Name the blood parasite species.
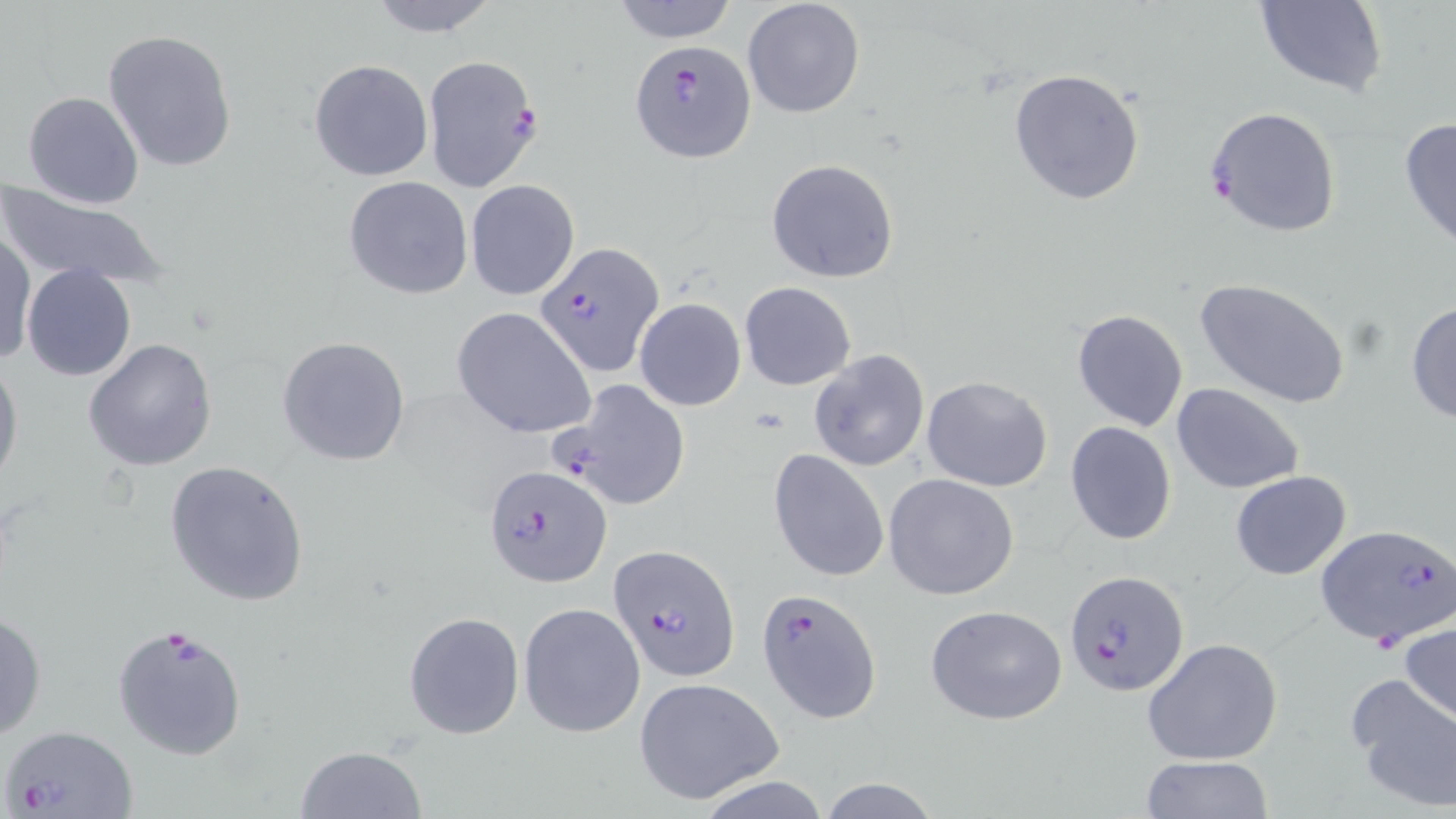
Plasmodium falciparum.

Summary:
  - Coordinate format: approximate bounding boxes as (x1, y1, x2, y2) in pixels
  - Plasmodium falciparum-infected red blood cell locations: (630, 40, 756, 164), (423, 55, 543, 194), (1203, 106, 1342, 238), (534, 241, 663, 376), (555, 381, 690, 510), (484, 464, 611, 589), (1315, 523, 1456, 647), (609, 544, 738, 683), (1066, 571, 1188, 696), (758, 588, 882, 723), (113, 623, 250, 762), (2, 725, 138, 816)
  - Uninfected red blood cell locations: (364, 0, 502, 37), (609, 0, 740, 43), (741, 0, 866, 119), (1252, 0, 1387, 98), (103, 29, 237, 175), (309, 59, 433, 181), (1008, 68, 1145, 204), (22, 92, 144, 208), (1398, 117, 1456, 252), (765, 158, 898, 283), (343, 176, 473, 300), (465, 178, 579, 301), (0, 185, 171, 290), (0, 231, 35, 367), (21, 264, 136, 382), (1195, 277, 1352, 410), (741, 281, 855, 390), (635, 298, 745, 412), (1407, 301, 1456, 425), (450, 307, 596, 439), (1071, 308, 1188, 433), (277, 335, 412, 467), (83, 337, 218, 472), (808, 349, 929, 473), (0, 356, 23, 494), (922, 375, 1054, 492), (1172, 383, 1306, 495), (1065, 421, 1178, 547), (768, 447, 890, 583), (166, 460, 311, 606), (1231, 470, 1353, 581), (884, 474, 1020, 600), (518, 602, 644, 738), (924, 605, 1068, 725), (0, 609, 47, 740), (403, 611, 525, 739), (1400, 619, 1456, 724), (1142, 636, 1283, 766), (1345, 672, 1456, 810), (634, 677, 784, 804), (294, 746, 427, 819), (1140, 756, 1275, 817), (694, 772, 832, 819), (818, 776, 941, 819)
  - Stain: May-Grünwald-Giemsa
  - Preparation: thin blood film
  - Image size: 1456×819 pixels
  - Field of view: single
  - Modality: optical microscopy
  - Magnification: 1000x